Locate and identify every blood parasite.
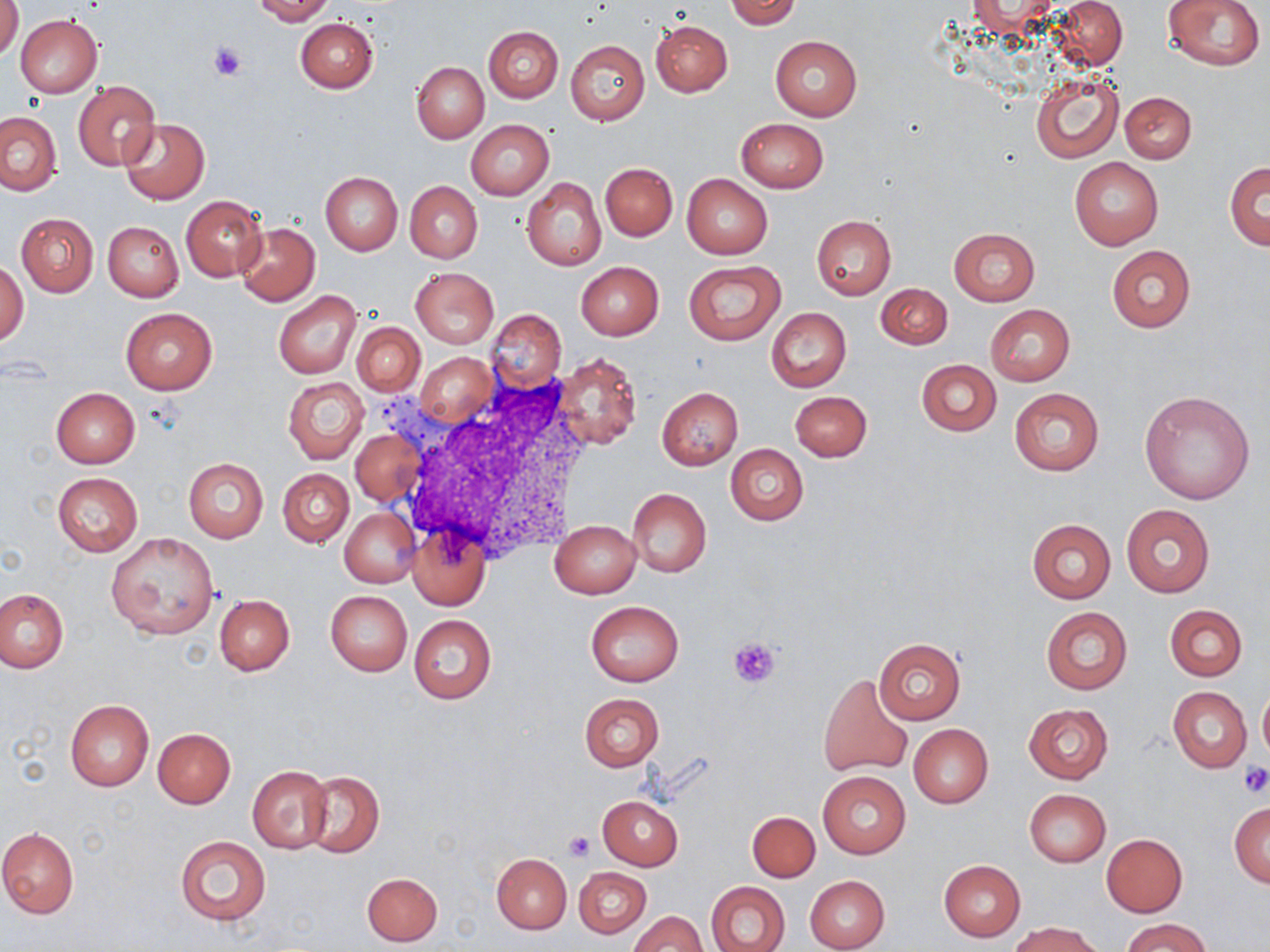

No blood parasites seen.

Summary:
  - Coordinate format: approximate bounding boxes as (x1,y1)-(x2,y2) corner pairs in pixels
  - White blood cell locations: (397,371)-(595,561)
  - Platelet locations: (209,42)-(247,80), (728,636)-(784,687), (1238,762)-(1270,797), (563,830)-(597,861)
  - Uninfected red blood cell locations: (1,0)-(24,61), (251,0)-(335,24), (726,0)-(801,29), (1162,0)-(1266,70), (1053,1)-(1128,68), (16,15)-(103,97), (295,18)-(378,93), (651,20)-(733,96), (483,26)-(563,101), (770,35)-(862,121), (566,40)-(649,125), (411,61)-(489,142), (1031,70)-(1123,163), (73,81)-(160,170), (1120,90)-(1196,162), (0,111)-(63,196), (736,117)-(829,192), (120,118)-(209,205), (466,120)-(553,200), (1069,156)-(1163,249), (600,162)-(677,241), (1226,162)-(1269,249), (320,172)-(402,255), (681,174)-(773,259), (523,178)-(606,271), (404,181)-(483,263), (181,196)-(265,281), (15,212)-(99,297), (812,217)-(896,299), (102,220)-(184,300), (235,223)-(320,305), (948,227)-(1040,306), (1106,245)-(1195,332), (1,259)-(28,345), (576,261)-(664,340), (684,261)-(785,345), (411,267)-(498,347), (876,283)-(952,349), (275,292)-(360,378), (985,305)-(1075,385), (120,307)-(218,396), (766,308)-(851,391), (486,309)-(566,390), (352,321)-(424,396), (552,352)-(643,452), (417,353)-(494,425), (916,359)-(1001,437), (283,375)-(369,464), (51,387)-(140,468), (657,387)-(742,470), (1008,387)-(1105,477), (1139,389)-(1256,504), (790,391)-(871,461), (350,427)-(425,506), (726,443)-(808,525), (184,458)-(267,542), (277,468)-(353,547), (53,472)-(142,557), (627,489)-(711,577), (1121,502)-(1216,598), (340,508)-(419,588), (1026,518)-(1116,604), (550,521)-(641,598), (407,526)-(491,610), (106,532)-(219,640), (0,589)-(68,672), (326,590)-(412,676), (215,594)-(295,675), (586,600)-(683,687), (1165,605)-(1247,681), (1041,606)-(1132,695), (408,614)-(497,704), (875,638)-(965,724), (818,673)-(913,777), (1259,685)-(1270,761), (1169,687)-(1251,772), (579,693)-(664,770), (65,700)-(154,791), (1023,703)-(1113,784), (908,723)-(993,809), (153,728)-(235,808), (246,766)-(330,854), (816,770)-(911,859), (302,772)-(384,858), (1024,789)-(1110,866), (597,793)-(684,870), (1229,803)-(1269,888), (747,811)-(820,882), (0,827)-(79,919), (1102,834)-(1187,916), (176,836)-(270,927), (492,853)-(572,933), (939,860)-(1025,941), (574,867)-(651,938), (361,872)-(443,946), (804,874)-(890,952), (707,881)-(791,952), (630,912)-(706,951), (1122,917)-(1213,952), (1011,922)-(1101,952)
  - Slide-level diagnosis: negative for blood parasites
  - Preparation: thin blood smear
  - Field of view: one of a larger specimen
  - Modality: light microscopy
  - Magnification: 1000x
  - Stain: May-Grünwald-Giemsa
  - Image size: 1270×952 pixels